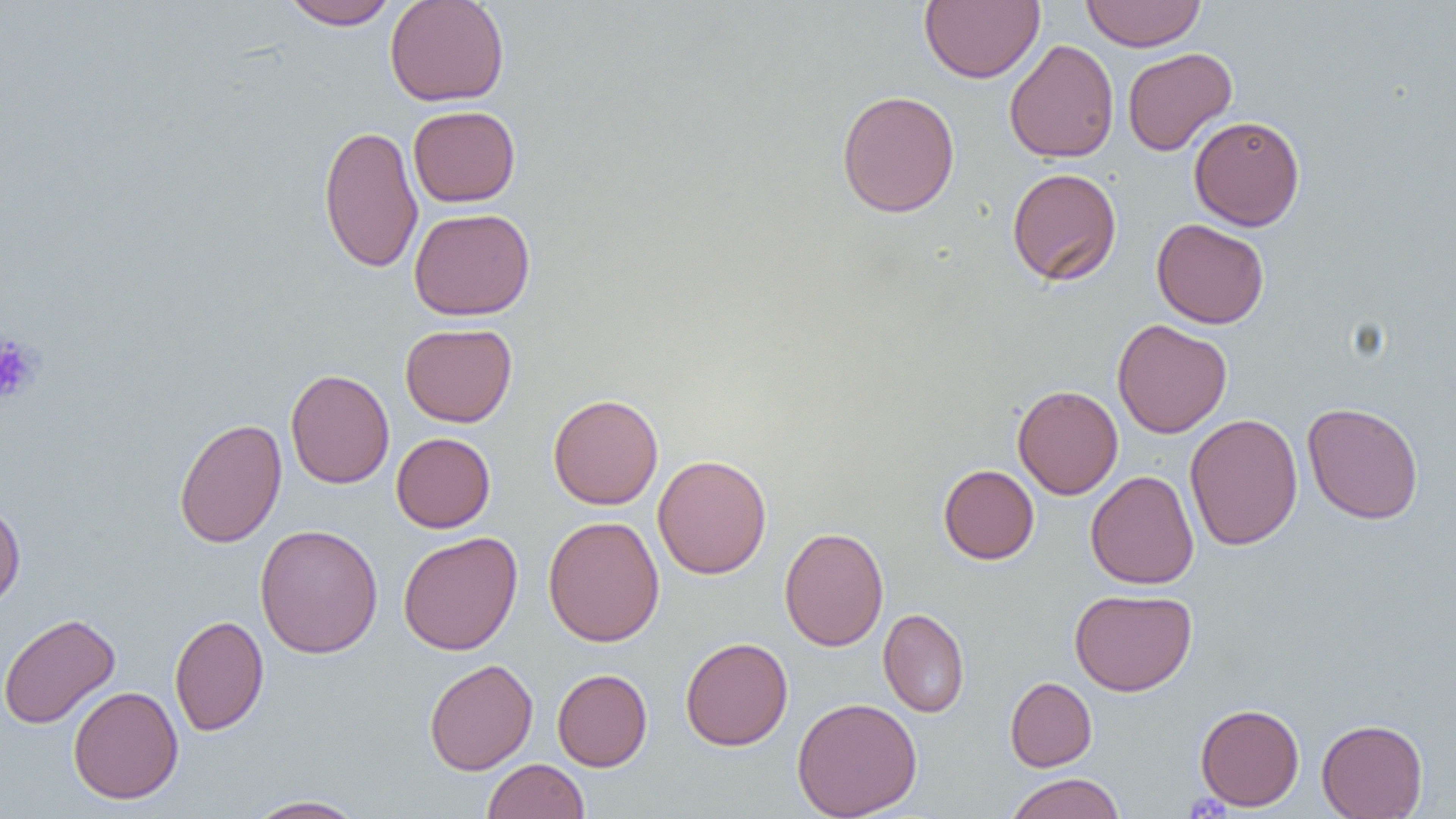

slide-level diagnosis = negative for blood parasites
preparation = thin blood film
platelet locations = approximate bounding boxes as (x1,y1)-(x2,y2) corner pairs in pixels: (0,333)-(43,405)
image size = 1456×819 pixels
field of view = one of a larger specimen
modality = light microscopy
uninfected red blood cell locations = approximate bounding boxes as (x1,y1)-(x2,y2) corner pairs in pixels: (384,0)-(510,107), (920,0)-(1044,84), (1080,0)-(1206,51), (281,1)-(400,30), (1004,39)-(1119,163), (1122,47)-(1237,156), (836,90)-(960,218), (408,105)-(520,207), (1189,115)-(1305,230), (319,124)-(424,274), (1006,167)-(1122,286), (409,207)-(536,320), (1151,218)-(1270,329), (1113,319)-(1232,438), (400,323)-(517,427), (285,368)-(394,489), (1013,384)-(1123,499), (548,393)-(663,510), (1302,402)-(1424,525), (1184,413)-(1303,551), (173,417)-(287,549), (391,432)-(495,533), (653,454)-(772,579), (938,464)-(1039,564), (1085,470)-(1199,589), (0,498)-(26,610), (543,515)-(665,647), (255,523)-(383,659), (779,526)-(889,652), (397,531)-(523,655), (1069,588)-(1197,696), (879,608)-(970,717), (0,612)-(120,729), (169,614)-(269,736), (680,636)-(793,751), (424,659)-(538,776), (552,668)-(652,771), (1005,677)-(1096,771), (68,686)-(184,804), (792,696)-(923,818), (1195,703)-(1304,810), (1317,718)-(1428,819), (482,758)-(589,819), (1004,773)-(1125,819), (244,794)-(369,818)
magnification = 1000x